Give the position of every Plasmodium parasite.
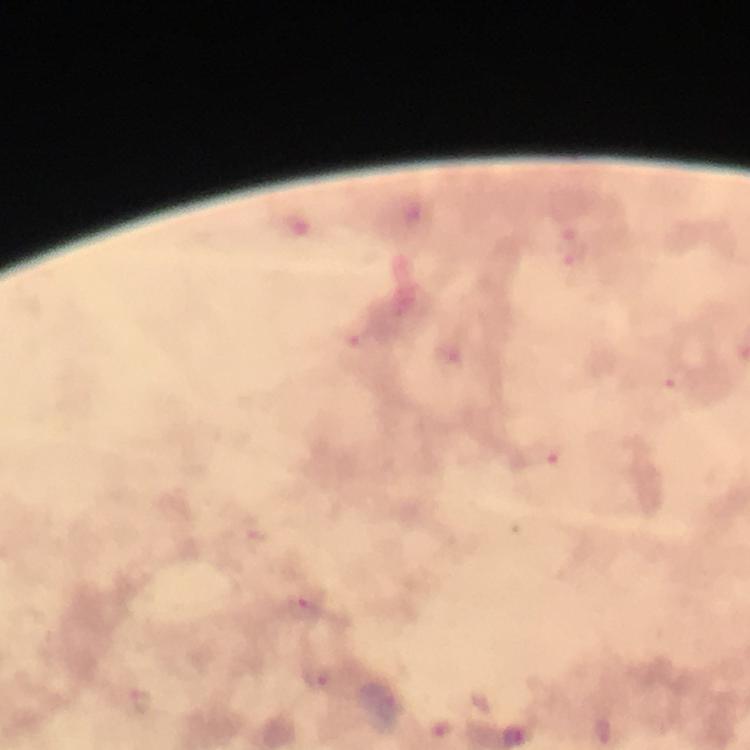

Approximate object centers, in pixels from the top-left corner.
Plasmodium parasites: (x=573, y=253), (x=364, y=345), (x=451, y=357), (x=676, y=379), (x=539, y=454), (x=305, y=607), (x=318, y=676), (x=389, y=708), (x=442, y=728).

Summary:
  - Cropped from: a single field of view
  - Context: from a malaria diagnostic workup
  - Magnification: 100x
  - Stain: Giemsa
  - Preparation: thick smear
  - Image size: 750×750 pixels
  - Immersion oil: applied
  - Capture: smartphone photograph through a microscope